Look for Plasmodium parasites.
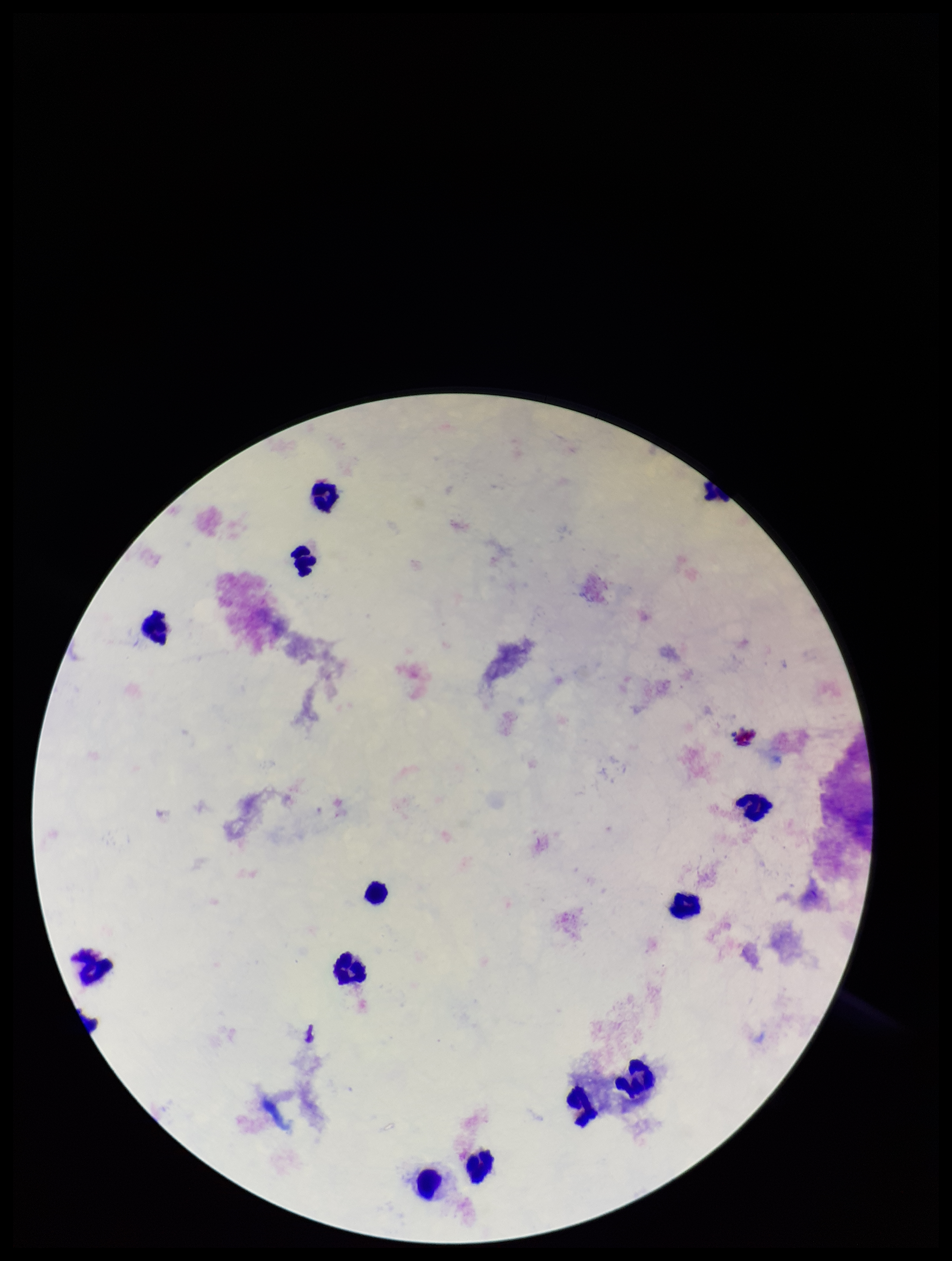

None detected.

Summary:
  - Parasite count: 0
  - Stain: Giemsa
  - Capture: smartphone photograph through the microscope eyepiece
  - Preparation: thick blood smear
  - Field of view: one from this slide
  - Patient malaria status: negative
  - Leukocyte count: 13
  - Image size: 952×1261 pixels